Classify this cell by malaria status.
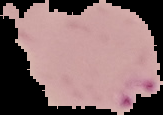
It is parasitized.

Summary:
  - Image size: 163×115 pixels
  - Preparation: thin blood smear
  - Image type: cell region segmented out of the field of view; surrounding area masked to black